Report the malaria status of this cell.
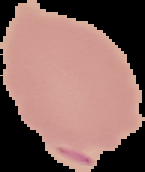

It is parasitized.

image size = 145×172 pixels
preparation = thin blood smear
image type = segmented cell region on a black background